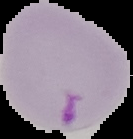

{
  "image_size": "133×139 pixels",
  "preparation": "thin blood smear",
  "result": "Plasmodium parasites detected",
  "image_type": "cell region segmented out of the field of view; surrounding area masked to black"
}